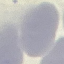

{
  "result": "no malaria parasites seen",
  "stain": "Giemsa",
  "preparation": "thin smear",
  "image_type": "automatically extracted cell patch, resized to 64 × 64 pixels",
  "capture": "smartphone camera at the microscope eyepiece"
}